Name the parasite shown.
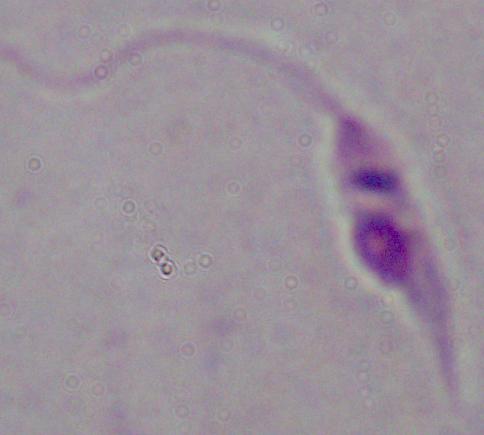

This is Leishmania.

Micrograph. Captured at 1000x magnification.